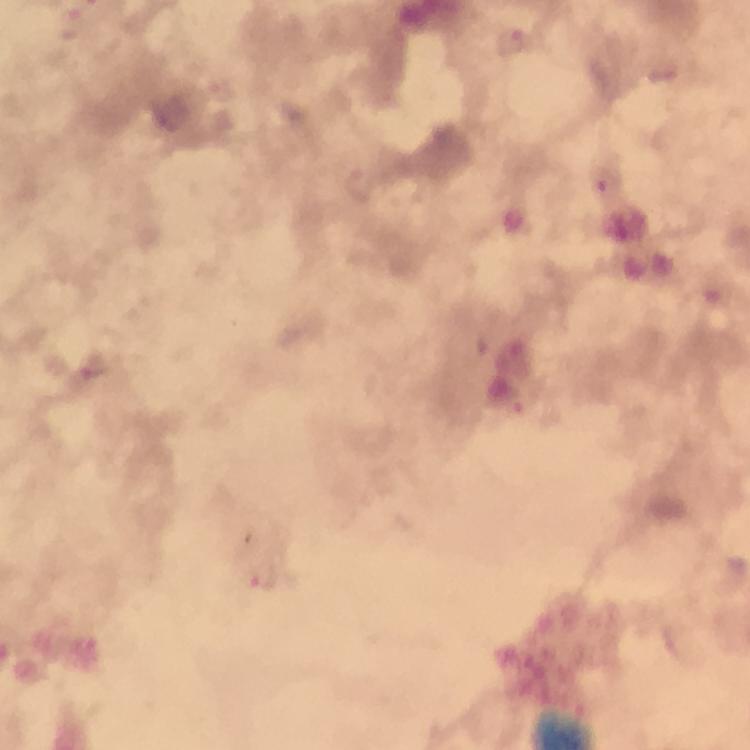
Approximate centers as {x, y} in pixels. Malaria parasite locations: {604, 177}, {263, 578}. A crop from one field of view. Immersion oil was used. Photographed through the microscope with a smartphone camera. Image is 750×750 pixels. From a diagnostic examination for malaria. 100x magnification. Thick smear. Giemsa-stained preparation.